Give the position of every malaria parasite.
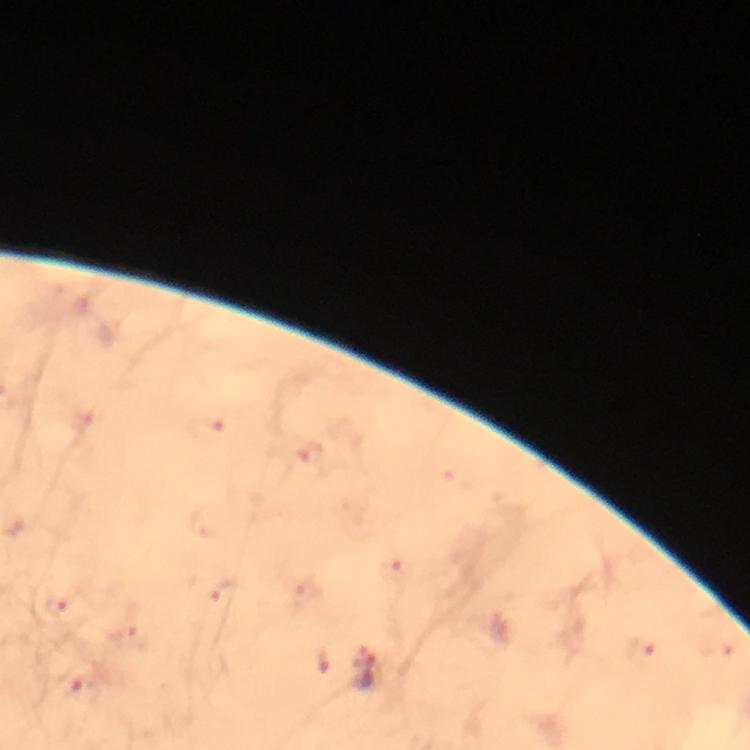
Approximate object centers, in pixels from the top-left corner.
Malaria parasites: (x=57, y=606), (x=367, y=671), (x=80, y=687).

Summary:
  - Magnification: 100x
  - Immersion oil: used
  - Capture: smartphone mounted on the microscope
  - Cropped from: one field of view
  - Image size: 750×750 pixels
  - Context: from a diagnostic examination for malaria
  - Stain: Giemsa
  - Preparation: thick blood film